Report the malaria status of this cell.
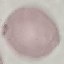
Uninfected.

Cell patch, automatically extracted from a larger field of view and resized to 64 × 64 pixels. Giemsa-stained preparation. Photographed with a smartphone camera at the microscope eyepiece. Thin smear of blood.